Report the malaria status of this cell.
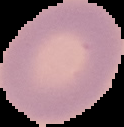
Uninfected.

Summary:
  - Image type: segmented cell region on a black background
  - Image size: 124×127 pixels
  - Preparation: thin blood film